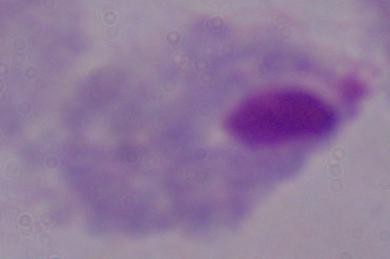 Photomicrograph. A trichomonad is shown. Captured at 1000x magnification.